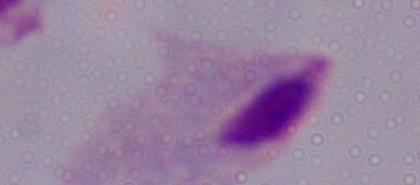

identification = trichomonad
magnification = 1000x
modality = micrograph